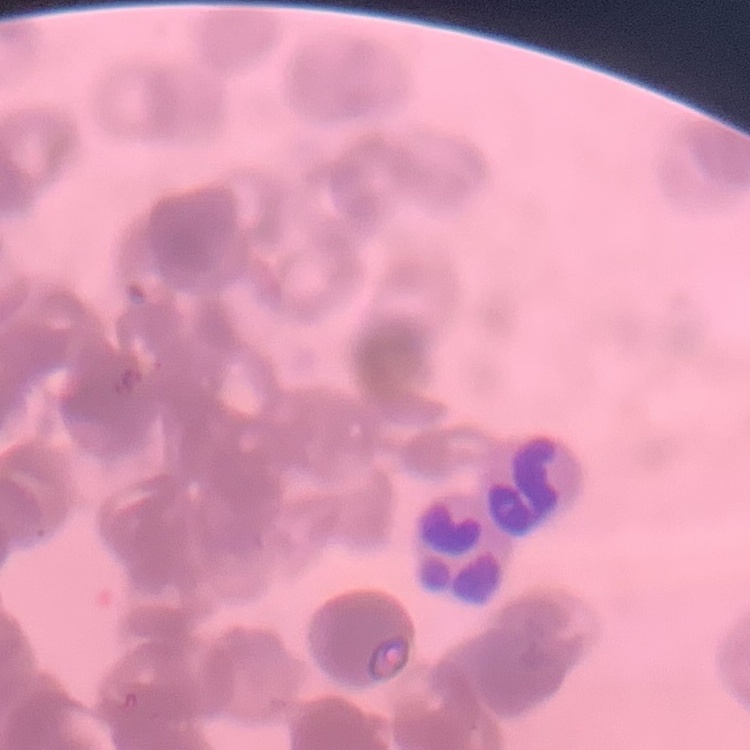

{
  "red_blood_cell_morphology": "rouleaux formation",
  "stain": "Field's or Giemsa",
  "preparation": "thin blood smear",
  "image_type": "one tile cut from a larger photomicrograph"
}